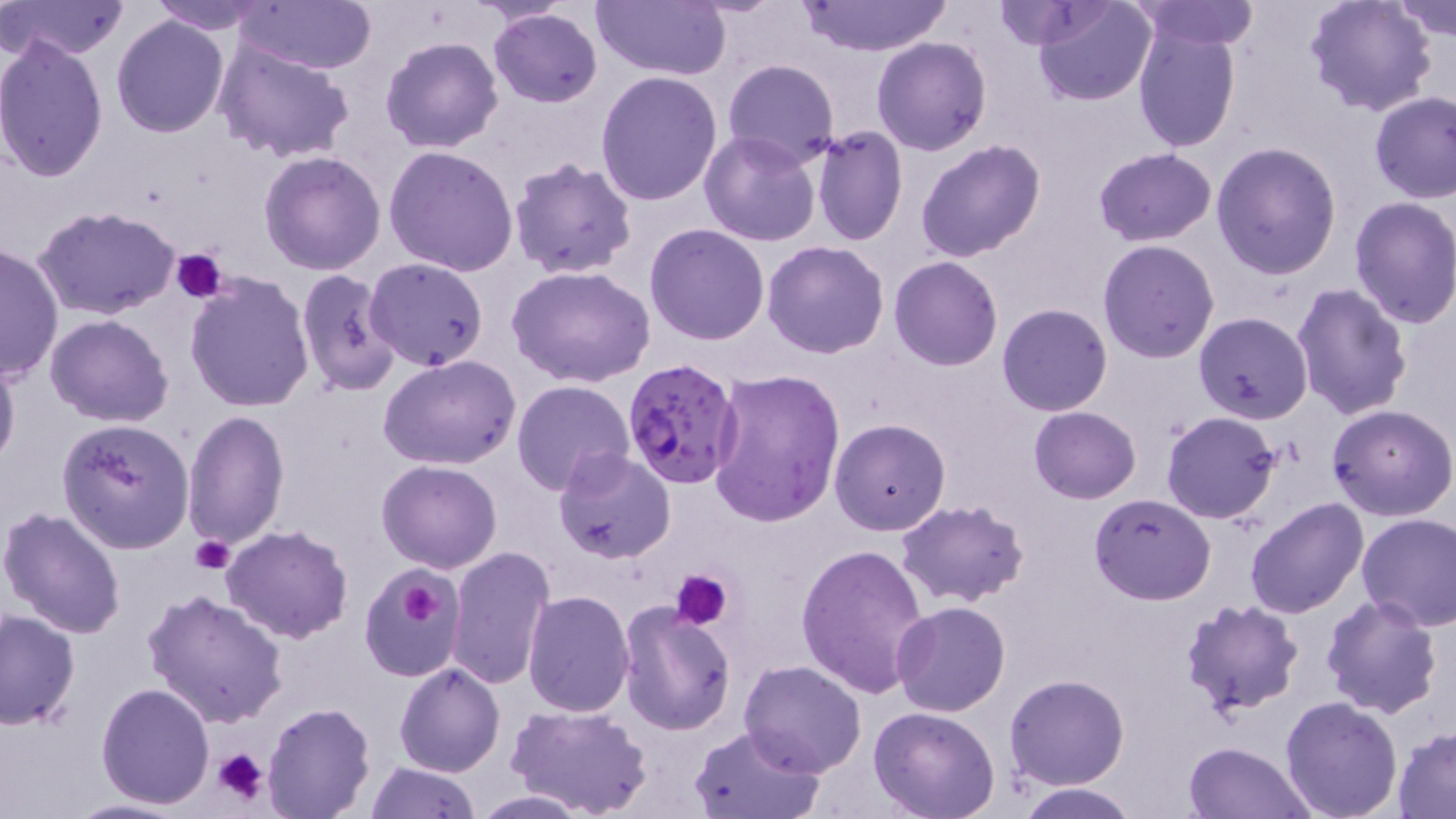

slide-level diagnosis = Plasmodium falciparum
preparation = thin blood film
image size = 1456×819 pixels
Plasmodium falciparum-infected red blood cell locations = approximate bounding boxes as (x1, y1, x2, y2) in pixels: (620, 357, 744, 487)
modality = light microscopy
platelet locations = approximate bounding boxes as (x1, y1, x2, y2) in pixels: (170, 248, 230, 303), (190, 534, 235, 574), (670, 568, 734, 631), (394, 569, 457, 634), (211, 747, 270, 808)
magnification = 1000x
stain = May-Grünwald-Giemsa
field of view = one of a larger specimen
uninfected red blood cell locations = approximate bounding boxes as (x1, y1, x2, y2) in pixels: (2, 0, 129, 64), (147, 0, 273, 33), (594, 0, 732, 81), (1032, 0, 1157, 106), (1304, 0, 1438, 117), (1390, 0, 1456, 42), (236, 1, 377, 74), (794, 1, 953, 56), (1132, 1, 1259, 50), (990, 2, 1109, 49), (488, 8, 602, 108), (111, 14, 229, 137), (1134, 24, 1241, 151), (0, 36, 109, 181), (212, 37, 354, 164), (380, 37, 504, 154), (871, 37, 992, 155), (722, 59, 841, 170), (596, 71, 723, 208), (1368, 91, 1456, 203), (811, 127, 908, 246), (698, 130, 821, 246), (915, 140, 1046, 263), (1211, 141, 1343, 280), (385, 146, 519, 278), (1095, 148, 1217, 246), (259, 152, 387, 275), (509, 157, 637, 279), (1349, 196, 1456, 329), (33, 205, 181, 322), (645, 223, 770, 346), (1097, 240, 1220, 363), (762, 241, 889, 359), (0, 242, 63, 383), (365, 257, 489, 370), (889, 257, 1002, 371), (509, 266, 657, 388), (295, 269, 400, 396), (184, 274, 315, 413), (1291, 282, 1413, 422), (996, 302, 1113, 417), (1194, 312, 1313, 423), (45, 315, 173, 425), (0, 348, 20, 476), (378, 354, 523, 471), (709, 368, 845, 525), (513, 379, 634, 495), (1327, 402, 1456, 520), (1028, 405, 1142, 504), (183, 410, 289, 549), (1160, 411, 1282, 524), (57, 418, 195, 553), (829, 419, 951, 536), (553, 447, 674, 564), (377, 460, 502, 573), (1089, 492, 1215, 606), (1243, 498, 1370, 619), (895, 500, 1031, 607), (0, 505, 127, 638), (1356, 512, 1456, 632), (221, 525, 352, 644), (796, 542, 931, 699), (446, 547, 553, 689), (359, 564, 464, 681), (143, 587, 289, 728), (521, 589, 635, 718), (1319, 593, 1442, 719), (1178, 599, 1305, 719), (618, 602, 737, 736), (891, 602, 1011, 716), (0, 610, 80, 730), (739, 660, 868, 776), (394, 663, 505, 777), (1005, 675, 1129, 789), (96, 682, 215, 807), (1278, 696, 1404, 819), (263, 702, 376, 819), (506, 702, 653, 819), (868, 707, 1001, 819), (689, 723, 824, 818), (1393, 728, 1456, 816), (1183, 740, 1313, 819), (365, 761, 479, 818), (1016, 781, 1139, 818), (469, 789, 594, 817), (62, 799, 193, 818)